State the blood parasite species.
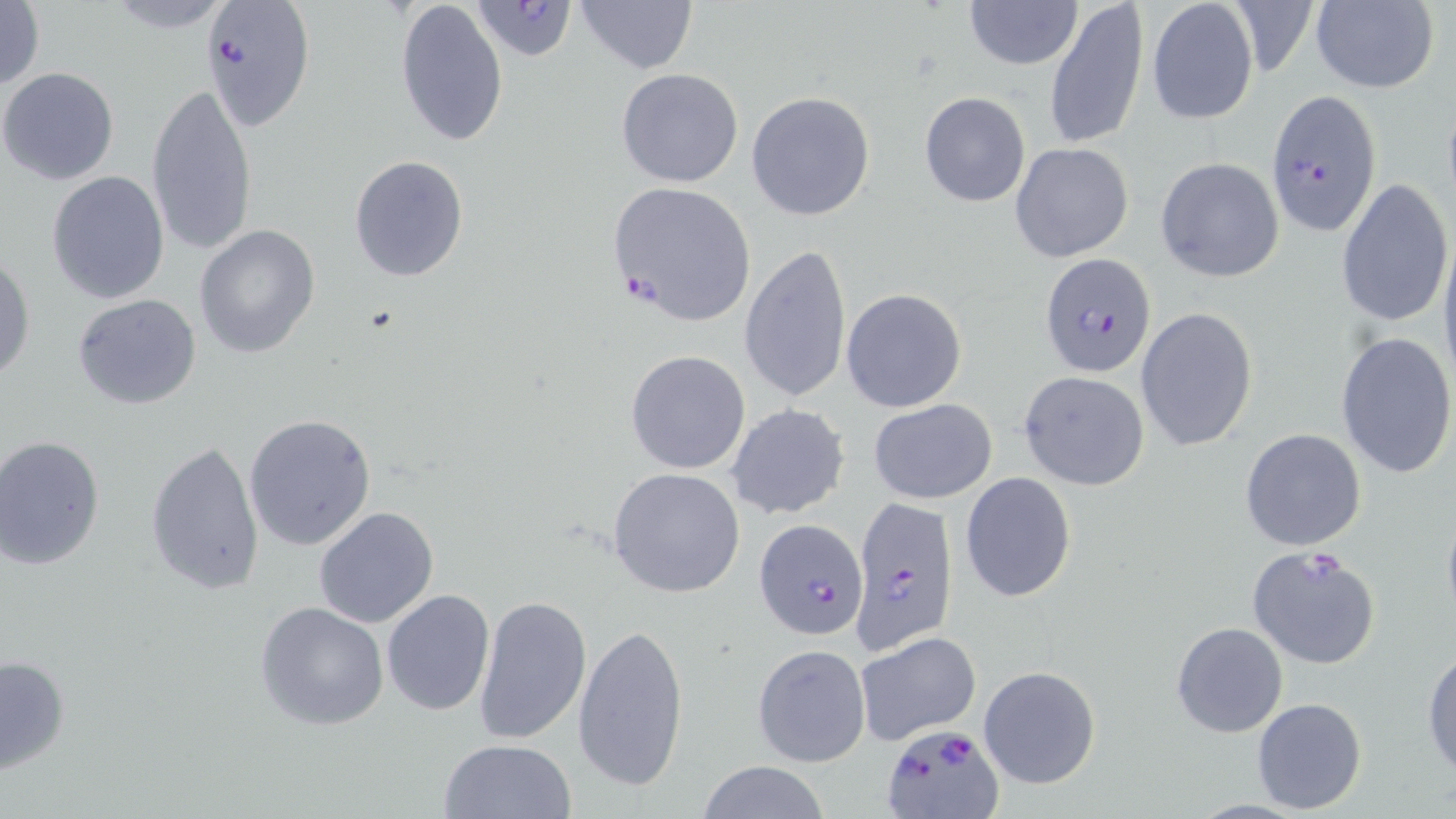
Plasmodium falciparum.

magnification = 1000x
image size = 1456×819 pixels
preparation = thin blood film
Plasmodium falciparum-infected red blood cell locations = approximate bounding boxes as (x1,y1)-(x2,y2) corner pairs in pixels: (202,0)-(316,131), (473,0)-(578,64), (1265,90)-(1383,236), (606,181)-(757,327), (1038,253)-(1157,378), (849,497)-(958,656), (752,514)-(865,643), (881,724)-(1001,818)
field of view = single
modality = optical microscopy
uninfected red blood cell locations = approximate bounding boxes as (x1,y1)-(x2,y2) corner pairs in pixels: (0,0)-(47,91), (394,0)-(508,148), (575,0)-(697,74), (1045,0)-(1149,151), (1309,0)-(1440,94), (963,1)-(1082,69), (1146,1)-(1259,126), (92,2)-(244,33), (0,67)-(120,186), (616,68)-(745,188), (146,79)-(257,256), (745,91)-(877,222), (919,93)-(1031,206), (1010,142)-(1134,263), (349,155)-(469,282), (1155,157)-(1286,283), (46,171)-(169,305), (1335,177)-(1452,330), (195,225)-(321,359), (1438,230)-(1456,391), (739,244)-(853,403), (0,250)-(35,385), (841,287)-(967,414), (72,294)-(202,409), (1135,307)-(1257,453), (1334,330)-(1455,480), (625,349)-(751,475), (1017,372)-(1149,491), (868,398)-(998,504), (727,403)-(849,520), (243,413)-(377,551), (1240,428)-(1367,551), (0,434)-(105,570), (145,438)-(266,595), (608,467)-(746,598), (958,472)-(1077,603), (1440,501)-(1456,632), (314,505)-(439,628), (1247,546)-(1381,671), (382,589)-(496,717), (474,594)-(593,745), (255,601)-(390,732), (574,621)-(690,790), (1171,621)-(1289,737), (854,632)-(982,746), (751,643)-(871,768), (1422,644)-(1456,778), (1,652)-(70,775), (978,666)-(1102,790), (1251,697)-(1367,815), (438,738)-(577,819), (694,762)-(833,818)
stain = May-Grünwald-Giemsa